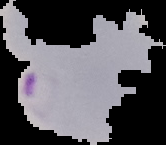
preparation = thin blood film
image type = cell region segmented out of the field of view; surrounding area masked to black
result = malaria parasites detected
image size = 166×145 pixels